Report the malaria status of this cell.
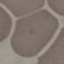
Uninfected.

Summary:
  - Image type: automatically extracted cell patch, resized to 64 × 64 pixels
  - Capture: smartphone through the microscope eyepiece
  - Preparation: thin blood smear
  - Stain: Giemsa